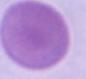
1000x magnification. An erythrocyte is seen. Photomicrograph.